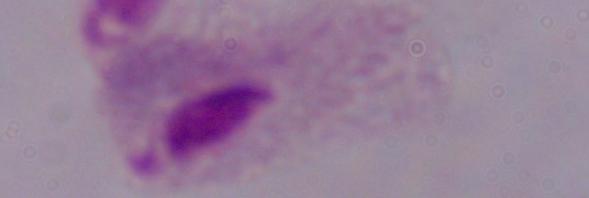

Captured at 1000x magnification. A trichomonad is seen. Micrograph.